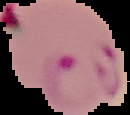

Summary:
  - Image type: cell region segmented out of the field of view; surrounding area masked to black
  - Preparation: thin blood film
  - Image size: 130×115 pixels
  - Result: malaria parasites identified